State which cell type is depicted.
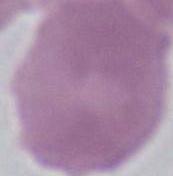

An erythrocyte.

Summary:
  - Modality: photomicrograph
  - Magnification: 1000x